Describe the morphology of the red blood cells.
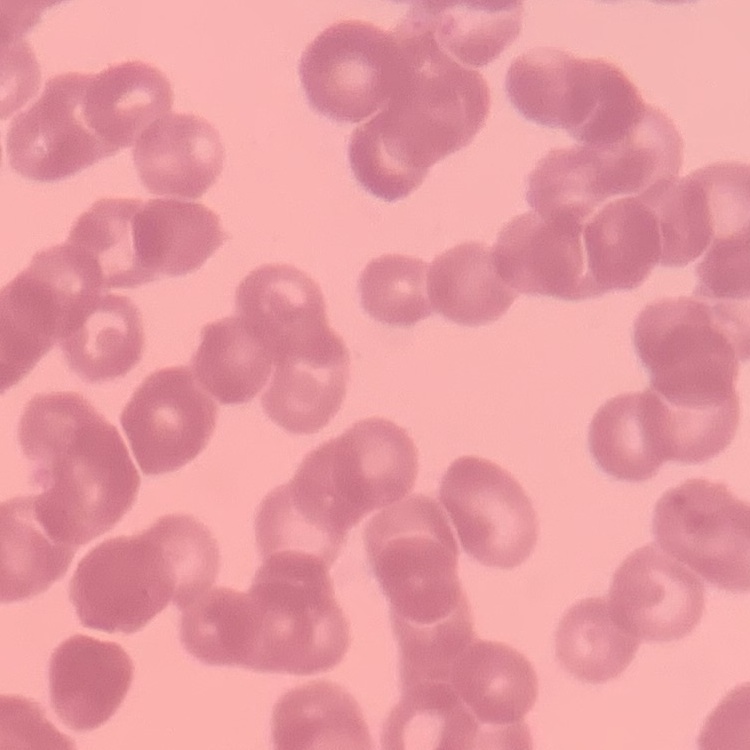
They show rouleaux formation.

Field's or Giemsa stain. One tile cut from a larger photomicrograph. Thin blood film.